Assess the morphology of the red blood cells.
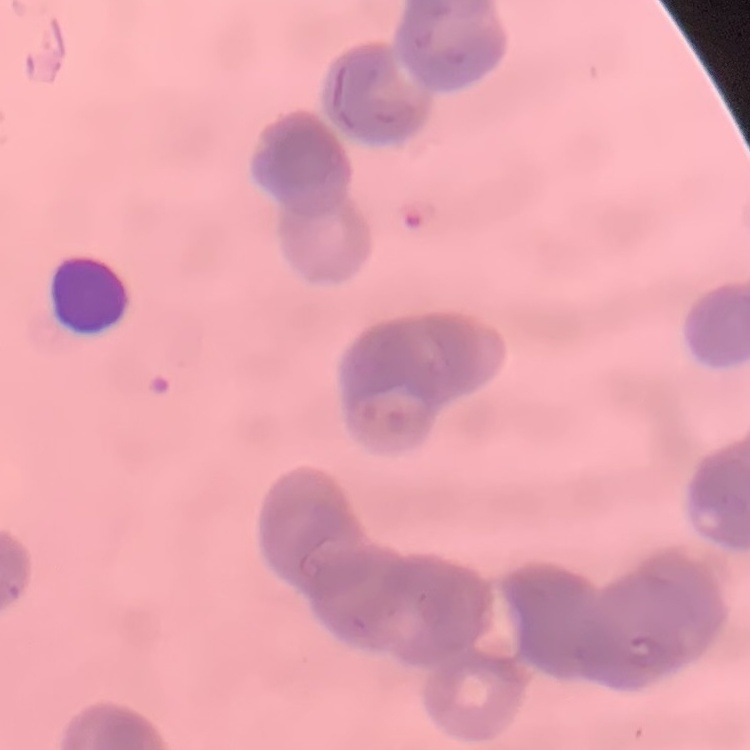
They show rouleaux formation.

{
  "preparation": "thin blood film",
  "image_type": "one tile cut from a larger photomicrograph",
  "stain": "Field's or Giemsa"
}